Classify this cell by malaria status.
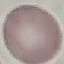

It is uninfected.

Photographed with a smartphone camera at the microscope eyepiece. Giemsa-stained preparation. Thin blood film. Cell patch, automatically extracted from a larger field of view and resized to 64 × 64 pixels.